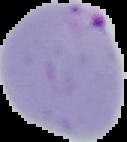
Summary:
  - Result: malaria parasites identified
  - Preparation: thin blood film
  - Image type: segmented cell region with the area outside set to black
  - Image size: 127×142 pixels